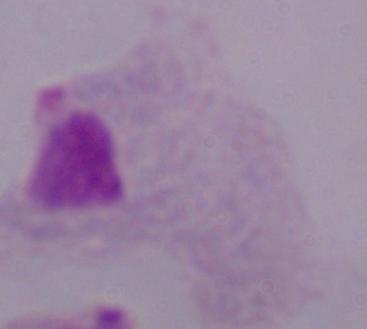

magnification: 1000x
modality: photomicrograph
identification: trichomonad